Report the malaria status of this cell.
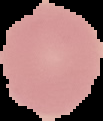
Uninfected.

Summary:
  - Image type: cell region segmented out of the field of view; surrounding area masked to black
  - Preparation: thin blood smear
  - Image size: 103×121 pixels